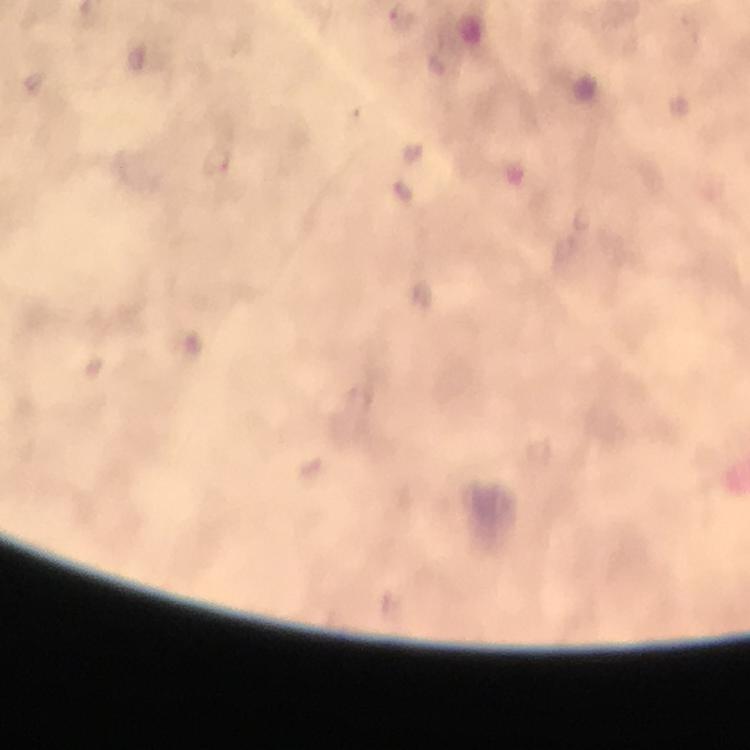
{
  "immersion_oil": "applied",
  "stain": "Giemsa",
  "image_size": "750×750 pixels",
  "cropped_from": "one field of view",
  "preparation": "thick blood film",
  "magnification": "100x",
  "malaria_parasite_locations": "approximate centers as {x, y} in pixels: {217, 160}",
  "context": "from a diagnostic examination for malaria",
  "capture": "smartphone photograph through a microscope"
}